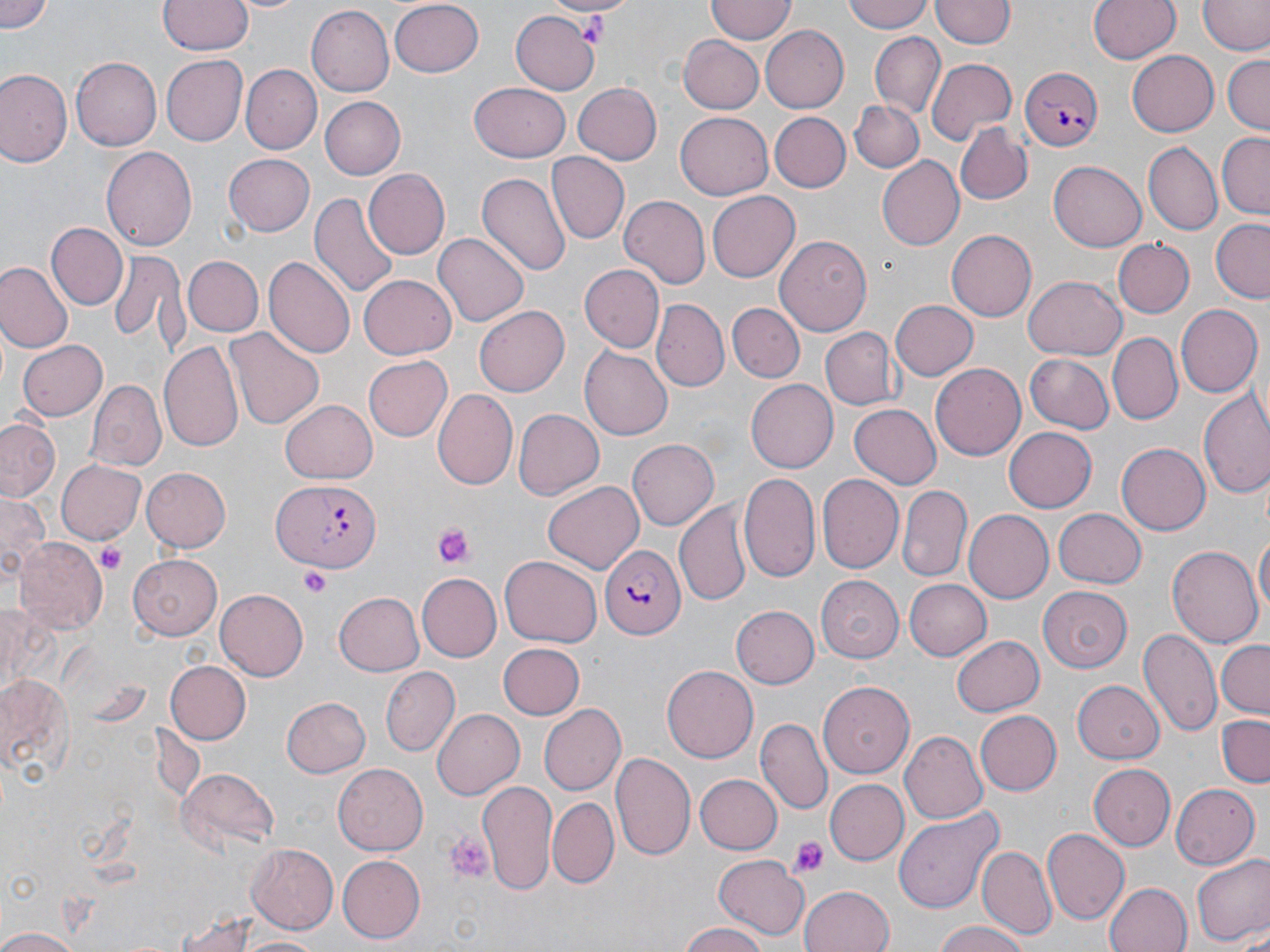 Approximate bounding boxes as (x1, y1, x2, y2) in pixels. Uninfected red blood cell locations: (2, 0, 53, 33), (159, 0, 251, 55), (707, 0, 796, 43), (844, 0, 933, 34), (1088, 0, 1180, 65), (390, 1, 484, 75), (932, 1, 1015, 49), (1201, 2, 1269, 56), (308, 5, 394, 96), (511, 8, 600, 94), (761, 26, 848, 112), (869, 33, 945, 114), (678, 35, 764, 115), (1127, 51, 1219, 137), (1222, 54, 1270, 134), (160, 55, 246, 147), (71, 56, 162, 152), (927, 57, 1018, 143), (241, 64, 320, 155), (0, 69, 72, 167), (471, 81, 569, 162), (573, 83, 661, 164), (317, 96, 406, 180), (848, 100, 922, 172), (770, 112, 850, 191), (675, 113, 773, 200), (956, 125, 1032, 204), (1215, 132, 1270, 220), (1142, 142, 1222, 236), (102, 145, 197, 254), (223, 151, 316, 236), (549, 152, 630, 244), (877, 157, 966, 250), (1049, 162, 1145, 250), (362, 169, 449, 261), (477, 173, 570, 278), (707, 189, 799, 279), (311, 191, 399, 300), (619, 195, 711, 289), (1211, 219, 1270, 304), (45, 221, 128, 310), (945, 230, 1036, 322), (435, 233, 528, 327), (774, 234, 872, 337), (1114, 239, 1194, 318), (107, 251, 187, 348), (264, 255, 354, 360), (184, 256, 265, 338), (0, 263, 72, 353), (580, 265, 665, 353), (357, 274, 456, 360), (1023, 275, 1125, 359), (888, 299, 977, 381), (653, 300, 729, 393), (730, 302, 803, 382), (475, 305, 569, 396), (1175, 305, 1261, 396), (229, 326, 325, 430), (820, 328, 901, 410), (1108, 333, 1182, 424), (158, 338, 245, 453), (16, 340, 108, 422), (579, 347, 672, 441), (1024, 354, 1115, 435), (361, 355, 451, 442), (929, 361, 1025, 457), (88, 379, 166, 470), (745, 380, 839, 473), (1197, 389, 1270, 499), (433, 390, 518, 491), (279, 399, 378, 485), (850, 403, 942, 488), (514, 408, 604, 500), (0, 418, 62, 501), (1003, 426, 1097, 514), (627, 438, 719, 531), (1116, 443, 1210, 536), (54, 459, 146, 545), (140, 467, 230, 552), (740, 473, 820, 581), (819, 474, 902, 572), (543, 480, 644, 575), (898, 486, 973, 583), (0, 492, 49, 580), (676, 500, 752, 605), (1053, 508, 1146, 589), (962, 509, 1053, 602), (1255, 529, 1269, 623), (15, 538, 106, 631), (1167, 546, 1262, 650), (130, 553, 226, 637), (500, 556, 602, 648), (416, 574, 501, 659), (815, 576, 904, 662), (904, 579, 991, 660), (1039, 586, 1131, 672), (217, 588, 308, 679), (333, 591, 425, 676), (729, 606, 818, 688), (1139, 627, 1221, 736), (951, 634, 1043, 717), (1214, 639, 1270, 719), (499, 643, 583, 720), (166, 662, 250, 742), (380, 665, 459, 756), (661, 666, 756, 762), (0, 669, 76, 783), (1073, 680, 1165, 765), (818, 681, 913, 777), (279, 696, 371, 777), (540, 705, 625, 792), (431, 707, 524, 800), (976, 710, 1062, 797), (1215, 714, 1270, 787), (758, 718, 830, 814), (900, 730, 988, 824), (613, 751, 696, 862), (1089, 764, 1175, 852), (333, 765, 428, 855), (177, 768, 279, 855), (696, 773, 781, 853), (823, 778, 907, 865), (475, 779, 560, 898), (1169, 783, 1258, 870), (548, 798, 617, 887), (896, 808, 1005, 915), (1041, 829, 1129, 924), (244, 842, 338, 933), (980, 847, 1054, 940), (335, 853, 424, 943), (1192, 853, 1270, 949), (714, 855, 811, 939), (1104, 881, 1192, 952), (799, 884, 896, 952), (172, 911, 286, 949), (931, 920, 1031, 952), (1233, 924, 1270, 952), (678, 925, 771, 952), (0, 926, 87, 952), (231, 933, 327, 952). Plasmodium falciparum-infected red blood cell locations: (1017, 65, 1101, 152), (273, 479, 381, 574), (598, 545, 686, 637). Platelet locations: (433, 523, 473, 568), (96, 542, 128, 576), (301, 567, 331, 598), (444, 828, 495, 883), (791, 837, 829, 878). Slide-level diagnosis: Plasmodium falciparum. May-Grünwald-Giemsa stain. Optical microscopy. Captured at 1000x magnification. Single field of view. Thin blood smear. Image is 1270×952 pixels.